Assess this cell for malaria.
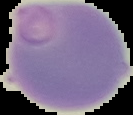
It is uninfected.

image type = segmented cell region on a black background
preparation = thin blood smear
image size = 133×115 pixels